Report the malaria status of this cell.
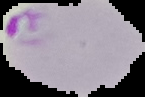
Parasitized.

Summary:
  - Preparation: thin blood film
  - Image size: 145×97 pixels
  - Image type: segmented cell region on a black background